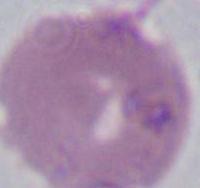 Photomicrograph. Captured at 1000x magnification. An erythrocyte is seen.